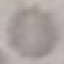

Summary:
  - Malaria status: uninfected
  - Stain: Giemsa
  - Preparation: thin blood smear
  - Image type: automatically extracted cell patch, resized to 64 × 64 pixels
  - Capture: smartphone camera at the microscope eyepiece